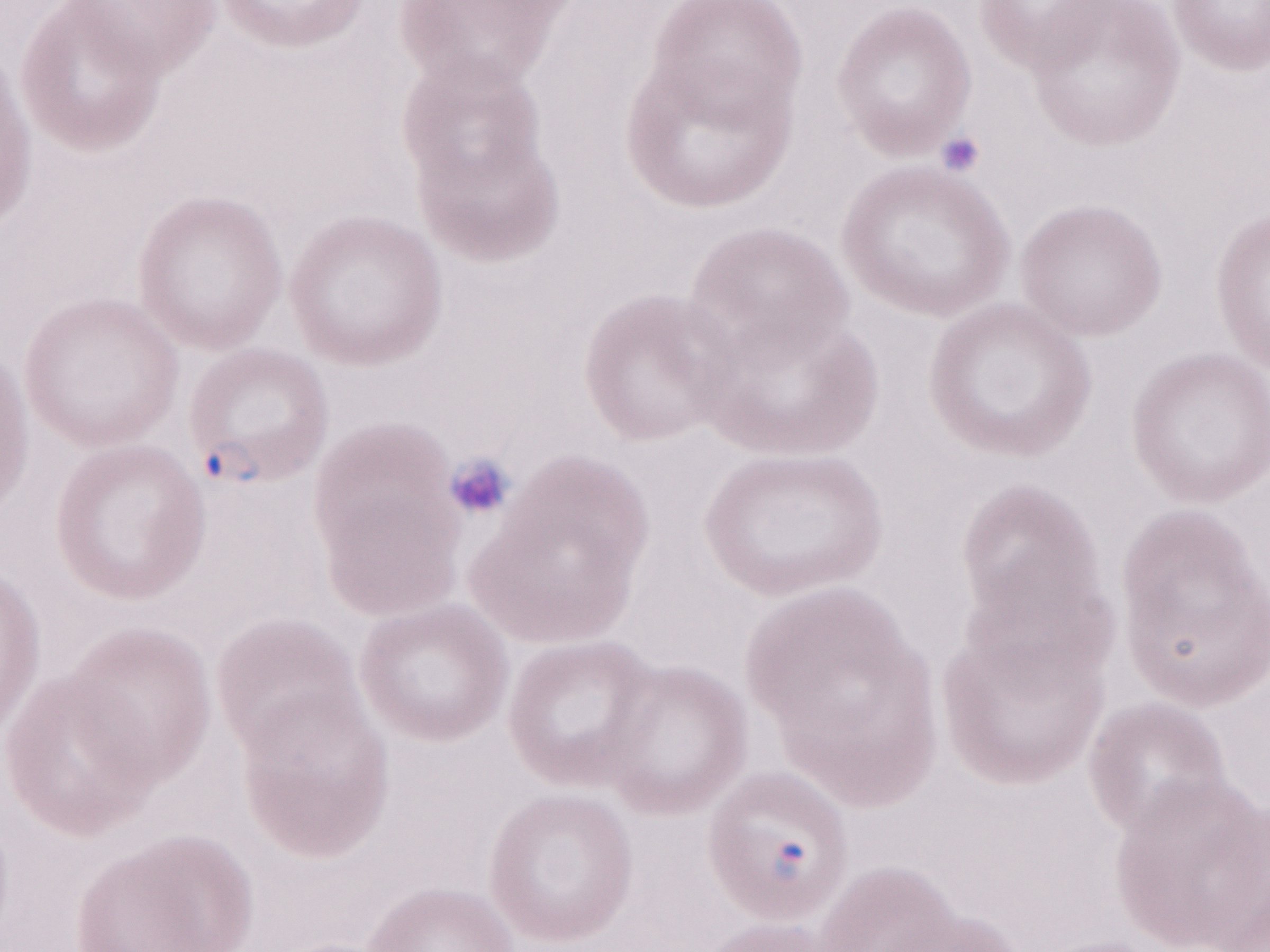

Patient-level malaria diagnosis: positive. May-Grünwald-Giemsa stain. Image is 1270×952 pixels. Olympus BX43 microscope, Olympus DP73 camera. Magnification: 1,000x. Thin peripheral-blood smear. Single field of view.